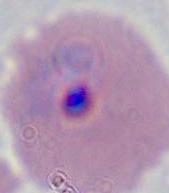 A Plasmodium parasite is shown. Captured at either 400x or 1000x magnification. Micrograph.